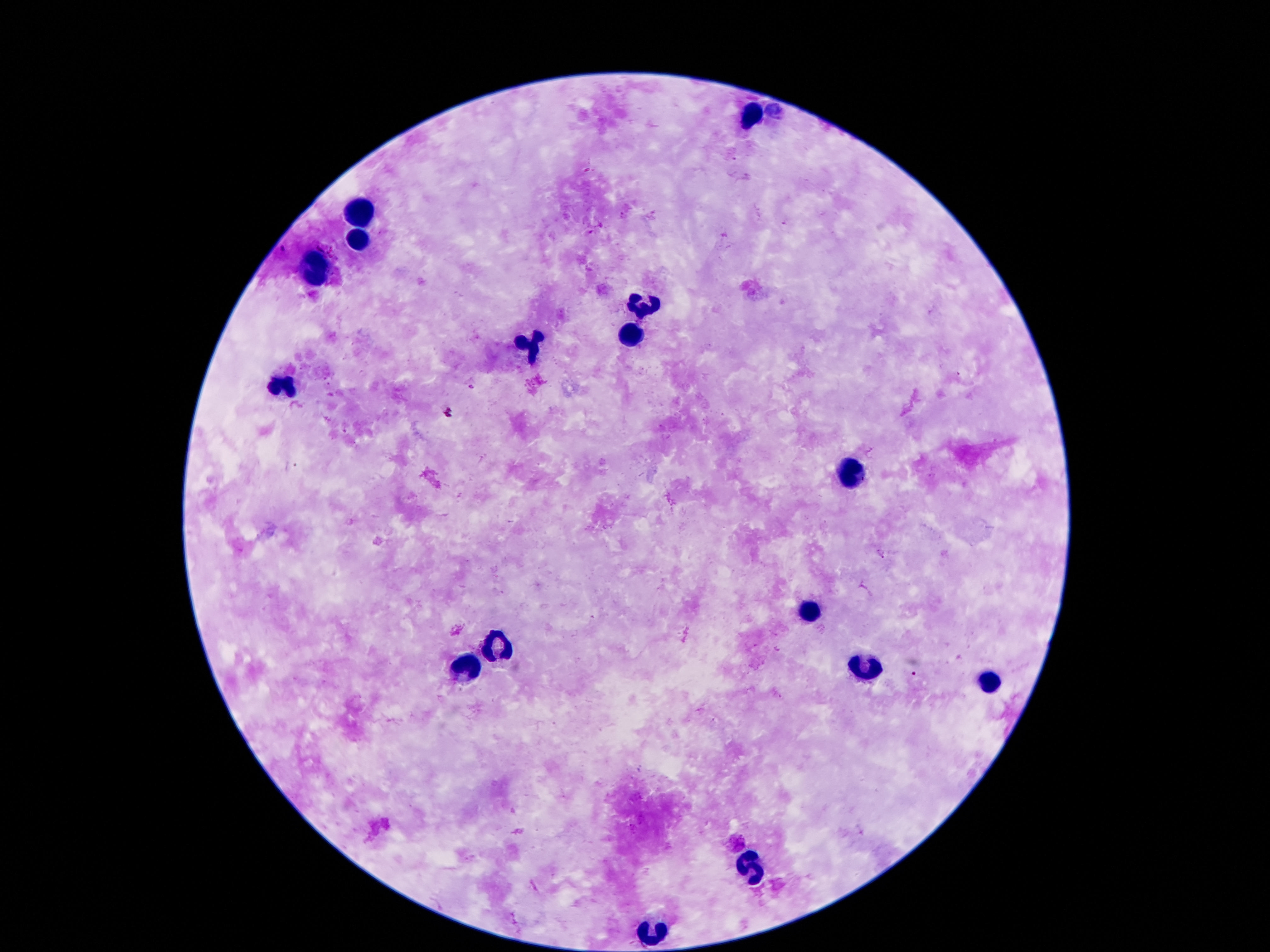
Approximate object centers, in pixels from the top-left corner. Leukocyte locations: (x=754, y=113), (x=360, y=214), (x=358, y=240), (x=316, y=271), (x=643, y=305), (x=633, y=336), (x=532, y=347), (x=282, y=387), (x=849, y=475), (x=807, y=613), (x=498, y=645), (x=467, y=666), (x=862, y=668), (x=988, y=683), (x=752, y=864), (x=652, y=934). Photographed through the microscope eyepiece with a smartphone camera. Patient malaria status: not infected. Image is 1270×952 pixels. Giemsa-stained preparation. 100x magnification. Thick blood film. One field from this slide.